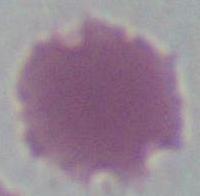

Summary:
  - Magnification: 1000x
  - Identification: erythrocyte
  - Modality: photomicrograph